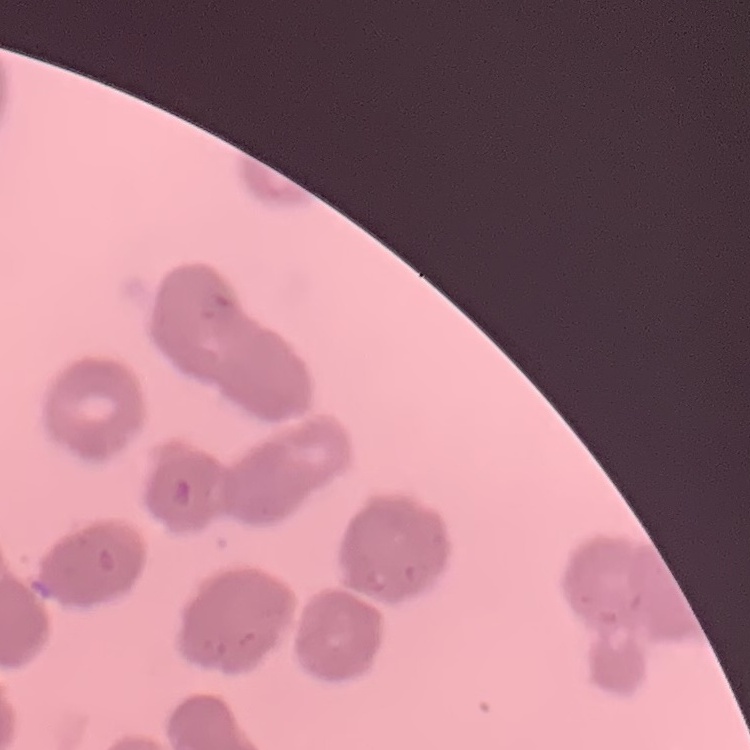
Summary:
  - Erythrocyte morphology: rouleaux formation
  - Preparation: thin peripheral smear
  - Image type: square crop of a larger photomicrograph
  - Stain: Field's or Giemsa